State which parasite is depicted.
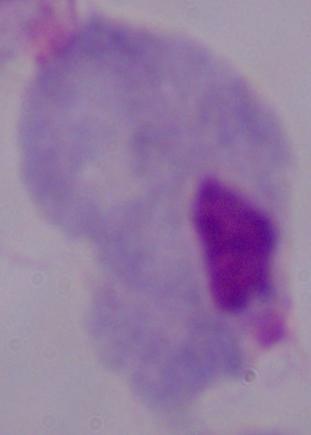

This is a trichomonad.

Summary:
  - Modality: photomicrograph
  - Magnification: 1000x